State the blood parasite species.
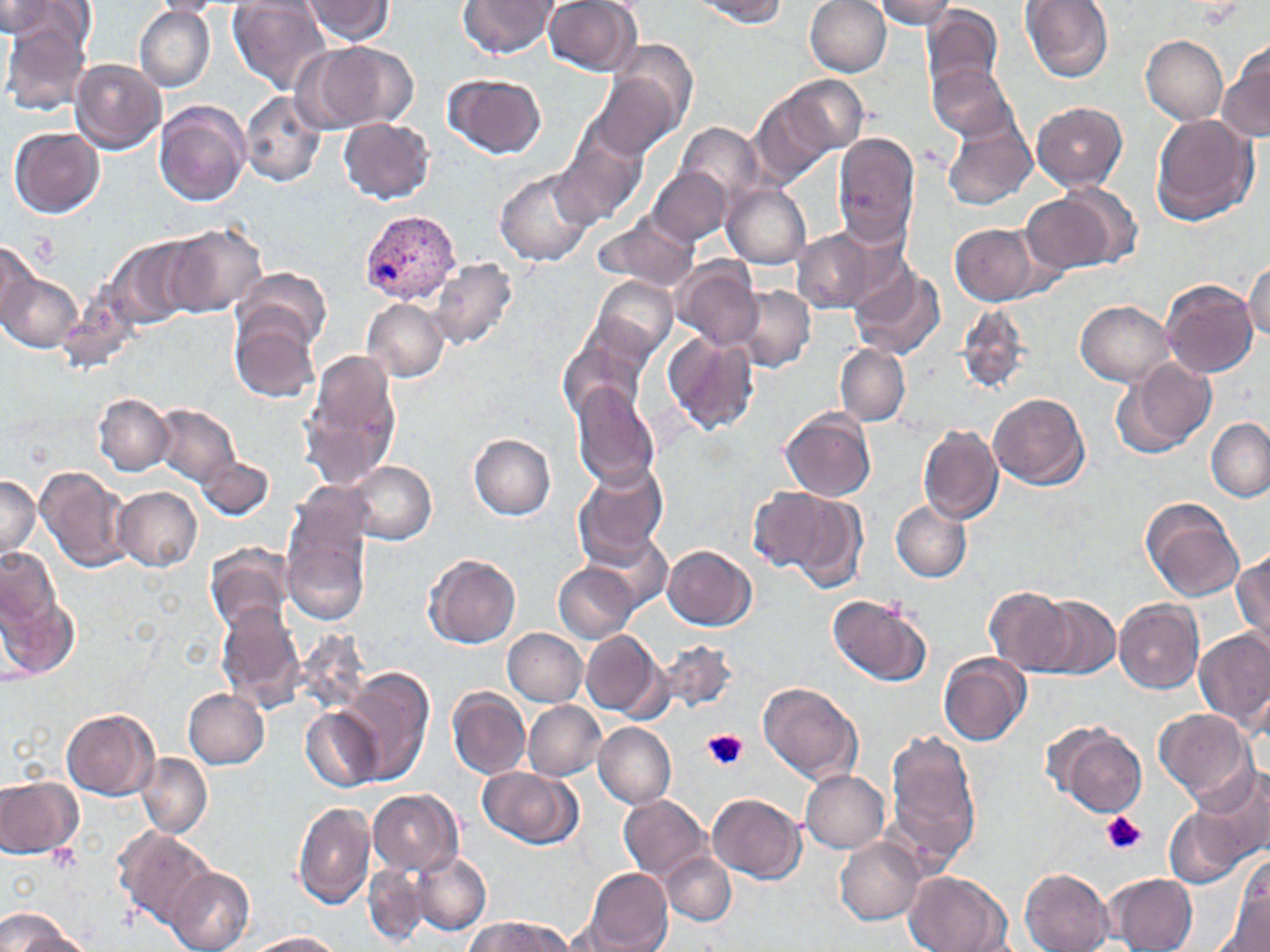

Plasmodium vivax.

Approximate bounding boxes as named x1/y1/x2/y2 corners in pixels. Uninfected red blood cell locations: (x1=145, y1=0, x2=226, y2=17), (x1=230, y1=0, x2=331, y2=95), (x1=459, y1=0, x2=560, y2=59), (x1=693, y1=0, x2=789, y2=26), (x1=805, y1=0, x2=891, y2=76), (x1=869, y1=0, x2=957, y2=29), (x1=302, y1=1, x2=396, y2=44), (x1=543, y1=1, x2=642, y2=75), (x1=1020, y1=1, x2=1115, y2=84), (x1=0, y1=2, x2=63, y2=40), (x1=920, y1=3, x2=1004, y2=96), (x1=1, y1=9, x2=93, y2=116), (x1=134, y1=9, x2=215, y2=91), (x1=1141, y1=35, x2=1228, y2=125), (x1=606, y1=37, x2=700, y2=144), (x1=293, y1=40, x2=418, y2=134), (x1=1219, y1=40, x2=1270, y2=144), (x1=71, y1=59, x2=166, y2=153), (x1=928, y1=60, x2=1021, y2=145), (x1=588, y1=71, x2=686, y2=164), (x1=444, y1=72, x2=548, y2=159), (x1=750, y1=79, x2=859, y2=179), (x1=240, y1=91, x2=325, y2=188), (x1=154, y1=101, x2=250, y2=206), (x1=1032, y1=101, x2=1127, y2=191), (x1=940, y1=112, x2=1039, y2=211), (x1=1151, y1=113, x2=1258, y2=226), (x1=340, y1=118, x2=435, y2=205), (x1=676, y1=122, x2=763, y2=204), (x1=9, y1=125, x2=104, y2=217), (x1=551, y1=132, x2=647, y2=229), (x1=832, y1=133, x2=921, y2=249), (x1=492, y1=167, x2=596, y2=267), (x1=649, y1=167, x2=733, y2=246), (x1=722, y1=183, x2=811, y2=268), (x1=1022, y1=188, x2=1132, y2=276), (x1=591, y1=215, x2=700, y2=294), (x1=949, y1=223, x2=1046, y2=307), (x1=162, y1=224, x2=266, y2=318), (x1=790, y1=226, x2=891, y2=314), (x1=104, y1=237, x2=204, y2=333), (x1=0, y1=242, x2=41, y2=330), (x1=430, y1=257, x2=517, y2=349), (x1=1245, y1=259, x2=1270, y2=341), (x1=674, y1=260, x2=762, y2=351), (x1=847, y1=260, x2=947, y2=362), (x1=235, y1=266, x2=333, y2=358), (x1=1, y1=271, x2=79, y2=353), (x1=590, y1=275, x2=678, y2=364), (x1=1163, y1=279, x2=1259, y2=376), (x1=735, y1=286, x2=815, y2=372), (x1=362, y1=298, x2=449, y2=382), (x1=1075, y1=301, x2=1174, y2=385), (x1=956, y1=304, x2=1028, y2=394), (x1=230, y1=311, x2=322, y2=404), (x1=560, y1=328, x2=653, y2=421), (x1=662, y1=332, x2=759, y2=436), (x1=836, y1=344, x2=909, y2=425), (x1=299, y1=347, x2=403, y2=492), (x1=1112, y1=357, x2=1217, y2=460), (x1=570, y1=381, x2=660, y2=489), (x1=989, y1=391, x2=1089, y2=488), (x1=93, y1=393, x2=173, y2=476), (x1=154, y1=405, x2=240, y2=485), (x1=780, y1=409, x2=877, y2=501), (x1=1207, y1=418, x2=1270, y2=502), (x1=917, y1=424, x2=1003, y2=525), (x1=470, y1=434, x2=555, y2=519), (x1=197, y1=452, x2=272, y2=521), (x1=346, y1=461, x2=435, y2=545), (x1=573, y1=461, x2=669, y2=567), (x1=34, y1=466, x2=132, y2=573), (x1=0, y1=474, x2=41, y2=562), (x1=112, y1=485, x2=201, y2=572), (x1=748, y1=486, x2=839, y2=574), (x1=790, y1=494, x2=868, y2=596), (x1=1140, y1=498, x2=1243, y2=602), (x1=281, y1=500, x2=374, y2=624), (x1=891, y1=501, x2=971, y2=582), (x1=588, y1=530, x2=672, y2=612), (x1=205, y1=542, x2=294, y2=635), (x1=663, y1=543, x2=757, y2=629), (x1=1, y1=545, x2=63, y2=636), (x1=1232, y1=546, x2=1270, y2=651), (x1=424, y1=554, x2=522, y2=649), (x1=554, y1=563, x2=639, y2=642), (x1=0, y1=579, x2=80, y2=681), (x1=983, y1=585, x2=1073, y2=675), (x1=828, y1=592, x2=933, y2=687), (x1=1032, y1=596, x2=1120, y2=680), (x1=1114, y1=598, x2=1204, y2=694), (x1=217, y1=603, x2=306, y2=709), (x1=503, y1=629, x2=588, y2=707), (x1=581, y1=629, x2=666, y2=720), (x1=1194, y1=629, x2=1270, y2=730), (x1=658, y1=639, x2=739, y2=716), (x1=939, y1=652, x2=1031, y2=747), (x1=342, y1=667, x2=434, y2=787), (x1=758, y1=681, x2=864, y2=784), (x1=448, y1=686, x2=530, y2=778), (x1=183, y1=689, x2=269, y2=768), (x1=524, y1=701, x2=606, y2=780), (x1=301, y1=707, x2=383, y2=792), (x1=62, y1=708, x2=160, y2=799), (x1=1154, y1=708, x2=1253, y2=800), (x1=593, y1=721, x2=675, y2=808), (x1=1049, y1=723, x2=1145, y2=816), (x1=882, y1=727, x2=981, y2=869), (x1=136, y1=753, x2=210, y2=838), (x1=1186, y1=764, x2=1270, y2=873), (x1=478, y1=766, x2=583, y2=850), (x1=801, y1=770, x2=890, y2=853), (x1=0, y1=776, x2=82, y2=860), (x1=368, y1=790, x2=463, y2=875), (x1=708, y1=792, x2=805, y2=883), (x1=619, y1=795, x2=713, y2=882), (x1=293, y1=800, x2=375, y2=910), (x1=1162, y1=803, x2=1257, y2=890), (x1=114, y1=826, x2=217, y2=932), (x1=836, y1=837, x2=925, y2=924), (x1=413, y1=851, x2=491, y2=935), (x1=662, y1=851, x2=735, y2=926), (x1=1233, y1=854, x2=1269, y2=947), (x1=363, y1=862, x2=432, y2=946), (x1=167, y1=868, x2=255, y2=952), (x1=585, y1=868, x2=672, y2=951), (x1=1020, y1=868, x2=1114, y2=951), (x1=903, y1=871, x2=1009, y2=952), (x1=1108, y1=873, x2=1197, y2=951), (x1=0, y1=908, x2=82, y2=952), (x1=461, y1=916, x2=575, y2=952), (x1=248, y1=932, x2=343, y2=951). Platelet locations: (x1=704, y1=730, x2=747, y2=771), (x1=1099, y1=811, x2=1145, y2=855). Plasmodium vivax-infected red blood cell locations: (x1=357, y1=210, x2=460, y2=305). Light microscopy. 1000x magnification. Image is 1270×952 pixels. Single field of view. May-Grünwald-Giemsa-stained preparation. Thin blood film.